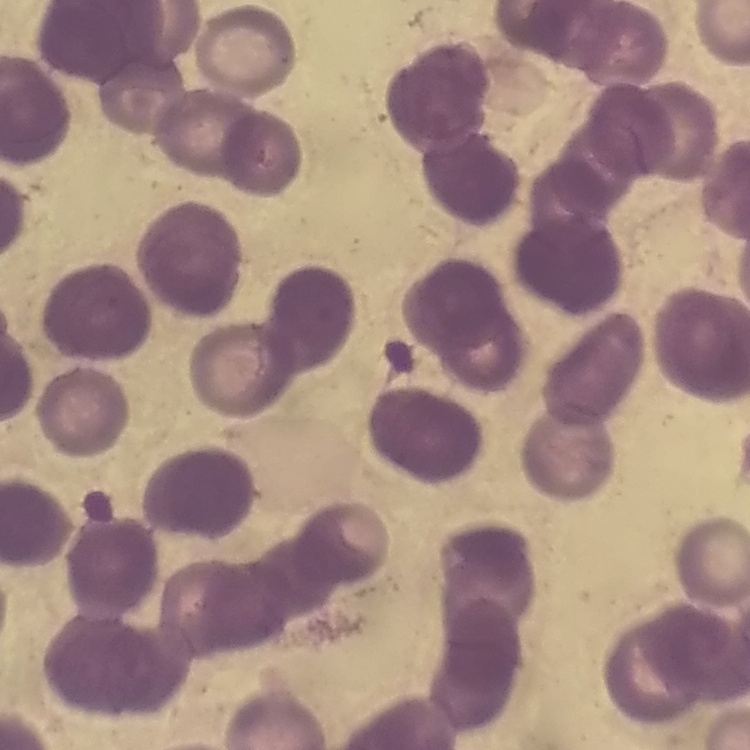
red blood cell morphology = rouleaux formation
image type = one tile cut from a larger photomicrograph
preparation = thin peripheral smear
stain = Field's or Giemsa